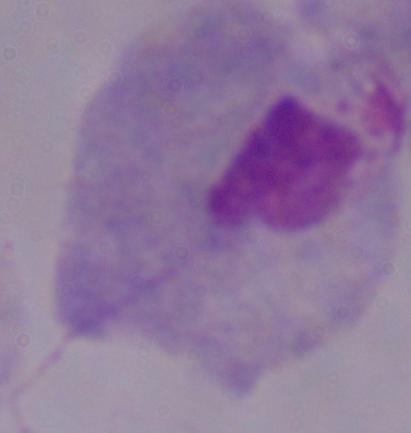
magnification = 1000x
modality = micrograph
identification = trichomonad